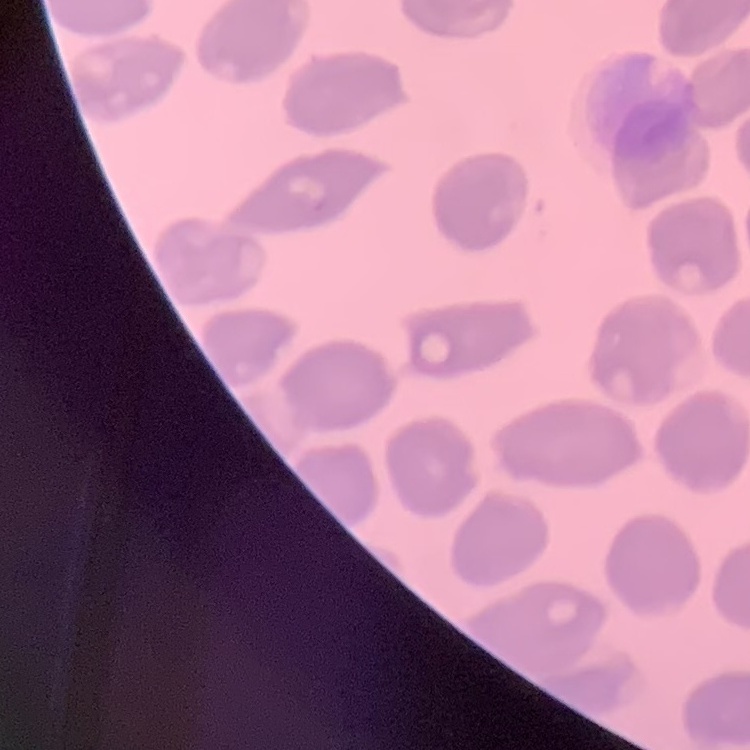 The red blood cells exhibit no rouleaux formation. One tile cut from a larger photomicrograph. Thin blood film. Field's or Giemsa stain.